State which cell type is depicted.
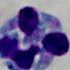
A leukocyte.

Captured at 1000x magnification. Photomicrograph.